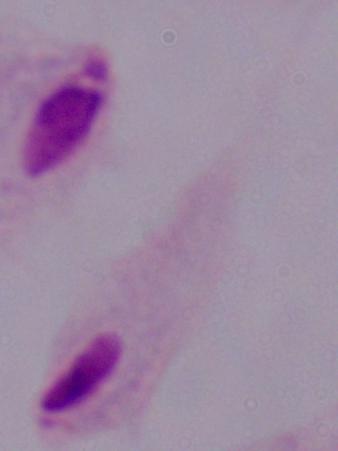
A trichomonad is seen. Captured at 1000x magnification. Micrograph.